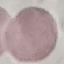 Malaria status: uninfected. Cell patch, automatically extracted from a larger field of view and resized to 64 × 64 pixels. Thin blood film. Giemsa-stained preparation. Acquired by smartphone through the microscope eyepiece.